Identify the parasite.
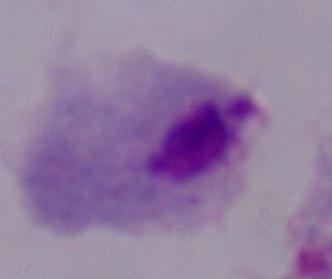
This is a trichomonad.

Summary:
  - Magnification: 1000x
  - Modality: photomicrograph